Identify the preparation type.
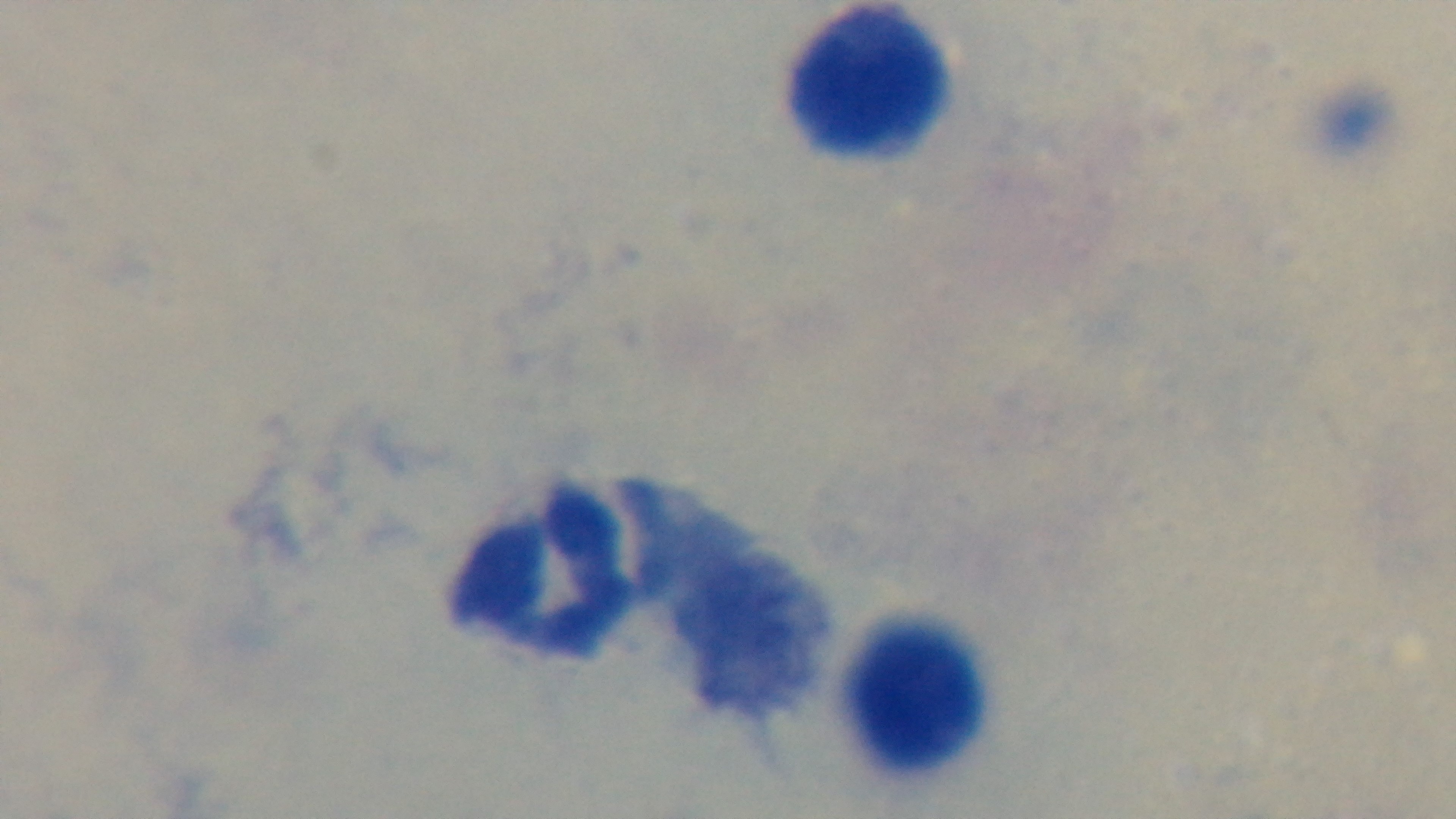
It is a thick blood film.

{
  "capture": "mounted 4K digital camera",
  "stain": "Giemsa",
  "malaria_status": "negative",
  "field_of_view": "one from the slide",
  "modality": "light microscopy",
  "objective": "100x oil immersion"
}